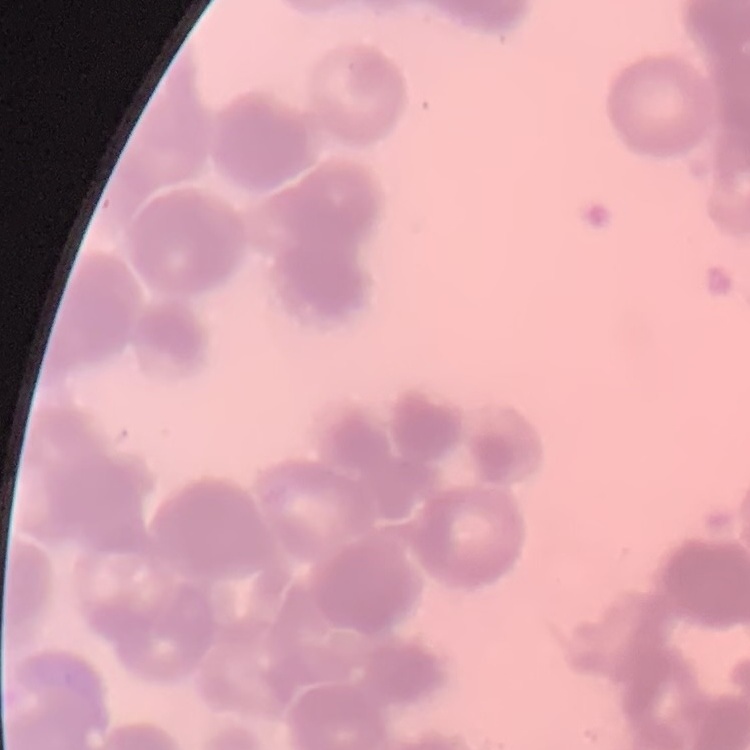
The red blood cells show rouleaux formation. Thin peripheral smear. Field's or Giemsa stain. One tile cut from a larger photomicrograph.